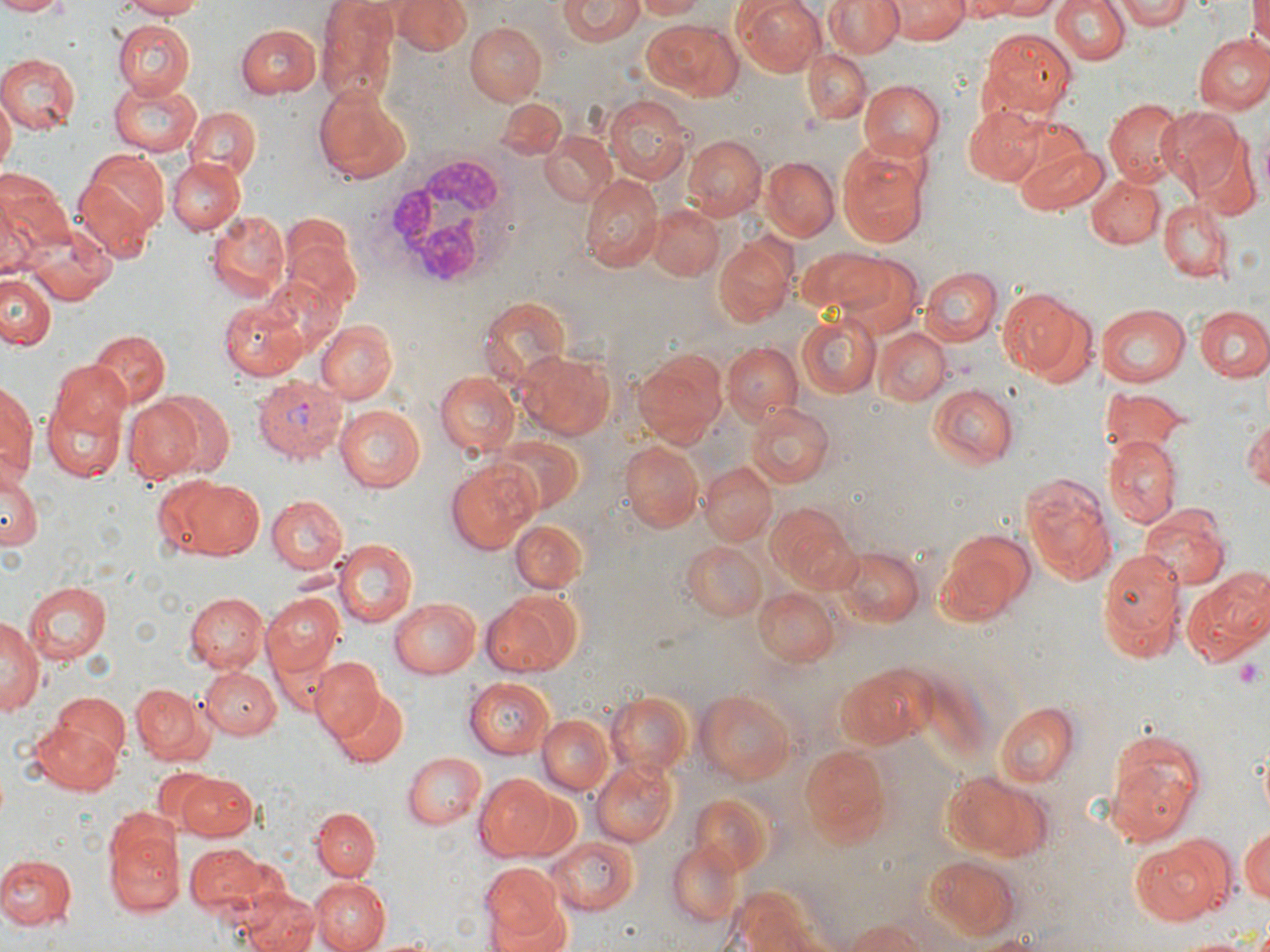

slide_level_diagnosis: Plasmodium vivax
magnification: 1000x
field_of_view: single
image_size: 1270×952 pixels
modality: optical microscopy
uninfected_red_blood_cell_locations: 'approximate bounding boxes as [x1, y1, x2, y2] in pixels: [0, 0, 67, 16], [114, 0, 208, 19], [314, 0, 402, 107], [394, 0, 470, 54], [634, 0, 706, 20], [737, 0, 829, 77], [826, 0, 902, 57], [963, 0, 1064, 19], [1114, 0, 1195, 28], [1250, 0, 1270, 54], [1051, 1, 1128, 66], [558, 2, 645, 45], [888, 3, 970, 44], [641, 18, 743, 101], [112, 20, 193, 97], [235, 22, 320, 97], [465, 22, 546, 106], [980, 29, 1075, 119], [1194, 32, 1270, 115], [803, 49, 870, 125], [0, 53, 80, 134], [110, 77, 205, 153], [857, 80, 944, 161], [313, 88, 412, 184], [0, 95, 15, 177], [605, 95, 691, 182], [496, 97, 567, 160], [1104, 99, 1184, 185], [187, 106, 259, 180], [961, 106, 1049, 185], [1154, 108, 1246, 195], [994, 114, 1093, 195], [541, 131, 619, 206], [683, 135, 765, 220], [1014, 144, 1108, 213], [1194, 144, 1262, 222], [837, 145, 928, 248], [75, 148, 168, 250], [166, 156, 244, 236], [759, 157, 840, 242], [0, 174, 71, 272], [578, 174, 662, 272], [1084, 174, 1163, 247], [1158, 201, 1231, 282], [648, 205, 725, 280], [204, 211, 289, 300], [26, 223, 117, 306], [713, 238, 796, 329], [797, 247, 901, 318], [830, 253, 924, 339], [918, 267, 1001, 347], [0, 274, 54, 351], [999, 285, 1095, 385], [482, 295, 573, 388], [219, 296, 315, 380], [1192, 303, 1268, 382], [1096, 304, 1189, 388], [796, 314, 882, 400], [316, 319, 398, 403], [874, 327, 951, 405], [90, 329, 170, 408], [725, 341, 800, 423], [633, 348, 729, 450], [518, 351, 615, 440], [50, 359, 133, 436], [435, 372, 520, 460], [1, 381, 36, 482], [926, 381, 1022, 471], [1102, 388, 1188, 456], [153, 389, 237, 480], [42, 394, 129, 484], [123, 397, 206, 483], [744, 400, 835, 488], [335, 404, 429, 492], [1243, 415, 1270, 490], [493, 435, 586, 513], [1104, 436, 1182, 528], [619, 440, 704, 532], [446, 462, 540, 552], [699, 462, 778, 546], [0, 470, 43, 552], [1023, 475, 1118, 588], [168, 477, 267, 560], [267, 494, 348, 574], [770, 505, 863, 591], [1138, 508, 1230, 591], [509, 519, 588, 594], [932, 529, 1035, 627], [332, 539, 418, 627], [680, 540, 768, 621], [837, 546, 924, 628], [1094, 549, 1186, 664], [1186, 567, 1270, 660], [26, 582, 112, 662], [753, 587, 840, 665], [481, 591, 587, 676], [185, 592, 267, 673], [263, 592, 343, 676], [389, 598, 481, 677], [0, 613, 41, 719], [312, 657, 383, 736], [835, 666, 933, 750], [201, 667, 279, 739], [463, 677, 555, 759], [130, 684, 211, 766], [332, 689, 410, 767], [608, 689, 693, 778], [695, 689, 797, 786], [36, 702, 129, 790], [994, 702, 1079, 787], [538, 715, 615, 795], [1104, 724, 1206, 845], [799, 741, 894, 848], [401, 750, 487, 830], [591, 759, 678, 847], [150, 768, 221, 832], [942, 772, 1054, 861], [175, 773, 257, 842], [473, 773, 557, 861], [689, 793, 776, 878], [313, 808, 380, 879], [102, 811, 184, 918], [1239, 824, 1270, 907], [548, 836, 639, 915], [1132, 838, 1231, 926], [666, 840, 741, 926], [185, 841, 267, 915], [0, 854, 77, 931], [924, 854, 1022, 942], [480, 863, 562, 945], [311, 877, 390, 952], [726, 885, 820, 952], [238, 886, 322, 952], [485, 900, 573, 951], [843, 919, 933, 952], [973, 933, 1051, 952], [1172, 934, 1258, 952]'
plasmodium_vivax_infected_red_blood_cell_locations: 'approximate bounding boxes as [x1, y1, x2, y2] in pixels: [253, 375, 351, 461]'
platelet_locations: 'approximate bounding boxes as [x1, y1, x2, y2] in pixels: [1234, 658, 1263, 686]'
stain: May-Grünwald-Giemsa
preparation: thin blood smear
white_blood_cell_locations: 'approximate bounding boxes as [x1, y1, x2, y2] in pixels: [370, 150, 522, 292]'